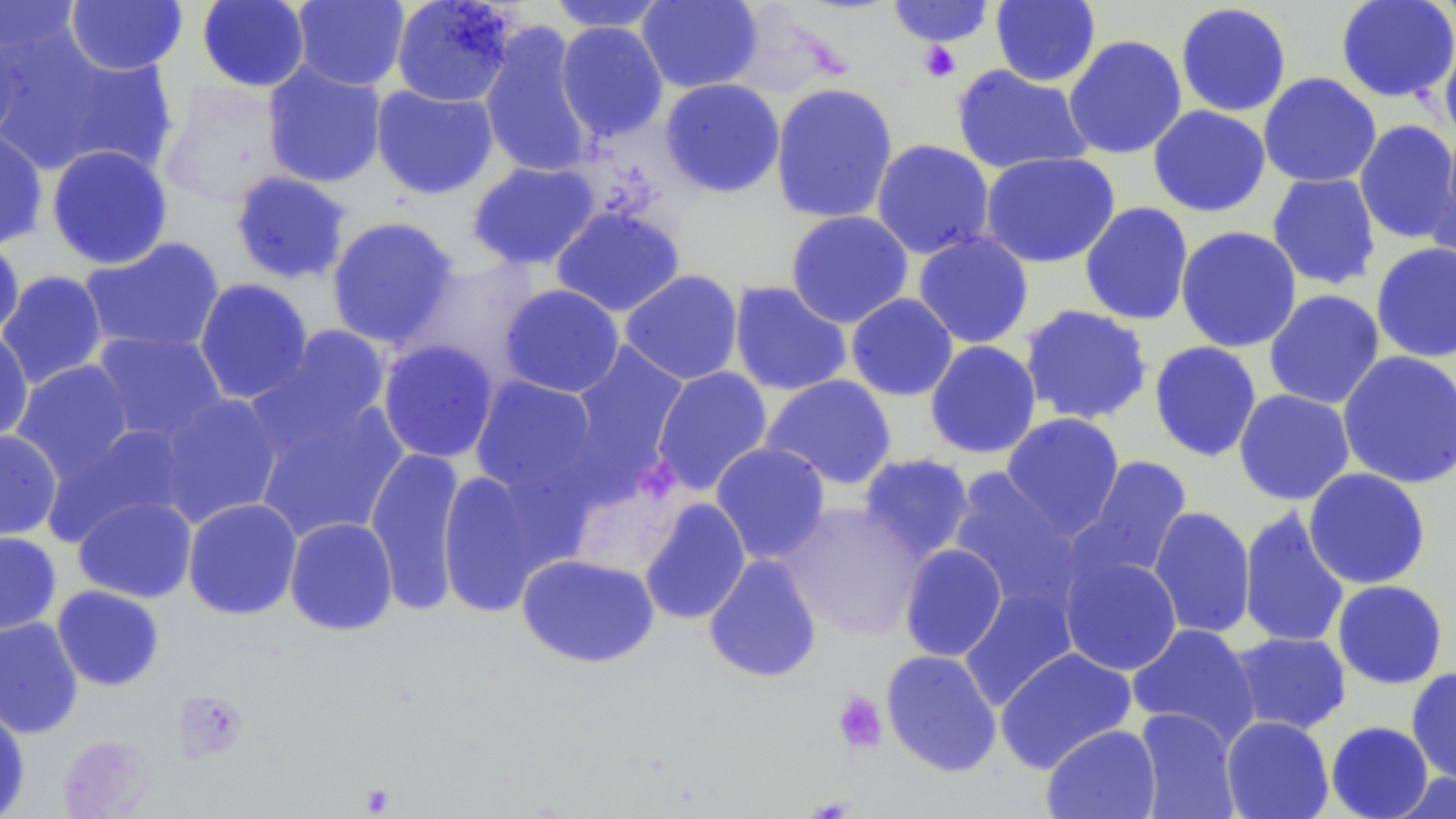
Summary:
  - Coordinate format: approximate bounding boxes as named x1/y1/x2/y2 corners in pixels
  - Uninfected red blood cell locations: (x1=0, y1=0, x2=83, y2=58), (x1=197, y1=0, x2=310, y2=93), (x1=291, y1=0, x2=410, y2=91), (x1=390, y1=0, x2=519, y2=107), (x1=636, y1=0, x2=762, y2=93), (x1=990, y1=0, x2=1101, y2=87), (x1=1335, y1=0, x2=1456, y2=104), (x1=1434, y1=0, x2=1456, y2=32), (x1=65, y1=1, x2=188, y2=75), (x1=545, y1=1, x2=672, y2=33), (x1=886, y1=1, x2=996, y2=47), (x1=1175, y1=3, x2=1292, y2=117), (x1=555, y1=21, x2=669, y2=141), (x1=0, y1=24, x2=29, y2=146), (x1=478, y1=24, x2=597, y2=179), (x1=1063, y1=34, x2=1187, y2=160), (x1=1439, y1=35, x2=1456, y2=147), (x1=12, y1=39, x2=178, y2=177), (x1=261, y1=61, x2=387, y2=189), (x1=951, y1=65, x2=1094, y2=175), (x1=1258, y1=72, x2=1382, y2=188), (x1=659, y1=78, x2=785, y2=198), (x1=158, y1=81, x2=290, y2=208), (x1=770, y1=82, x2=898, y2=224), (x1=371, y1=84, x2=498, y2=199), (x1=1148, y1=105, x2=1271, y2=217), (x1=1353, y1=120, x2=1456, y2=245), (x1=0, y1=125, x2=48, y2=251), (x1=870, y1=139, x2=995, y2=260), (x1=1424, y1=142, x2=1456, y2=274), (x1=46, y1=145, x2=174, y2=270), (x1=979, y1=152, x2=1120, y2=268), (x1=467, y1=162, x2=600, y2=270), (x1=230, y1=171, x2=353, y2=284), (x1=1266, y1=172, x2=1381, y2=290), (x1=1079, y1=202, x2=1194, y2=326), (x1=551, y1=205, x2=685, y2=317), (x1=785, y1=210, x2=914, y2=328), (x1=325, y1=216, x2=460, y2=350), (x1=1175, y1=225, x2=1302, y2=353), (x1=0, y1=232, x2=25, y2=343), (x1=913, y1=232, x2=1034, y2=348), (x1=79, y1=237, x2=226, y2=356), (x1=1371, y1=242, x2=1456, y2=363), (x1=407, y1=256, x2=544, y2=382), (x1=619, y1=269, x2=744, y2=385), (x1=0, y1=271, x2=109, y2=389), (x1=194, y1=278, x2=313, y2=405), (x1=728, y1=280, x2=852, y2=396), (x1=499, y1=284, x2=625, y2=397), (x1=1263, y1=289, x2=1385, y2=409), (x1=845, y1=293, x2=959, y2=401), (x1=1019, y1=304, x2=1153, y2=425), (x1=259, y1=325, x2=394, y2=443), (x1=0, y1=327, x2=34, y2=445), (x1=91, y1=330, x2=228, y2=443), (x1=377, y1=339, x2=500, y2=463), (x1=924, y1=340, x2=1042, y2=459), (x1=1149, y1=341, x2=1262, y2=462), (x1=568, y1=342, x2=690, y2=480), (x1=1337, y1=351, x2=1456, y2=490), (x1=11, y1=360, x2=136, y2=482), (x1=651, y1=366, x2=773, y2=496), (x1=760, y1=375, x2=897, y2=491), (x1=468, y1=376, x2=604, y2=505), (x1=1233, y1=389, x2=1355, y2=505), (x1=153, y1=392, x2=285, y2=527), (x1=249, y1=392, x2=409, y2=543), (x1=1001, y1=413, x2=1125, y2=537), (x1=47, y1=424, x2=194, y2=543), (x1=0, y1=430, x2=63, y2=542), (x1=710, y1=442, x2=830, y2=564), (x1=364, y1=445, x2=467, y2=615), (x1=857, y1=453, x2=976, y2=562), (x1=1077, y1=455, x2=1193, y2=580), (x1=436, y1=468, x2=556, y2=618), (x1=1303, y1=468, x2=1431, y2=590), (x1=947, y1=469, x2=1084, y2=612), (x1=565, y1=472, x2=689, y2=580), (x1=73, y1=495, x2=197, y2=603), (x1=638, y1=497, x2=751, y2=625), (x1=182, y1=498, x2=303, y2=620), (x1=778, y1=501, x2=927, y2=641), (x1=1148, y1=506, x2=1256, y2=640), (x1=1238, y1=506, x2=1351, y2=649), (x1=284, y1=517, x2=398, y2=636), (x1=0, y1=531, x2=62, y2=635), (x1=899, y1=543, x2=1008, y2=662), (x1=516, y1=553, x2=660, y2=668), (x1=703, y1=554, x2=822, y2=683), (x1=1059, y1=554, x2=1183, y2=676), (x1=1332, y1=580, x2=1448, y2=689), (x1=958, y1=584, x2=1080, y2=710), (x1=51, y1=586, x2=165, y2=691), (x1=0, y1=616, x2=84, y2=739), (x1=1127, y1=623, x2=1260, y2=745), (x1=1228, y1=631, x2=1352, y2=735), (x1=995, y1=648, x2=1137, y2=773), (x1=881, y1=649, x2=1002, y2=778), (x1=1406, y1=667, x2=1456, y2=786), (x1=0, y1=702, x2=30, y2=819), (x1=1133, y1=708, x2=1241, y2=819), (x1=1220, y1=715, x2=1334, y2=819), (x1=1325, y1=721, x2=1433, y2=819), (x1=1041, y1=724, x2=1161, y2=819), (x1=58, y1=735, x2=157, y2=818), (x1=1388, y1=772, x2=1456, y2=818)
  - Platelet locations: (x1=916, y1=40, x2=962, y2=83), (x1=832, y1=690, x2=888, y2=754)
  - Slide-level diagnosis: negative for blood parasites
  - Field of view: single
  - Stain: May-Grünwald-Giemsa
  - Modality: light microscopy
  - Magnification: 1000x
  - Preparation: thin blood smear
  - Image size: 1456×819 pixels